Outline each Plasmodium falciparum-infected red blood cell.
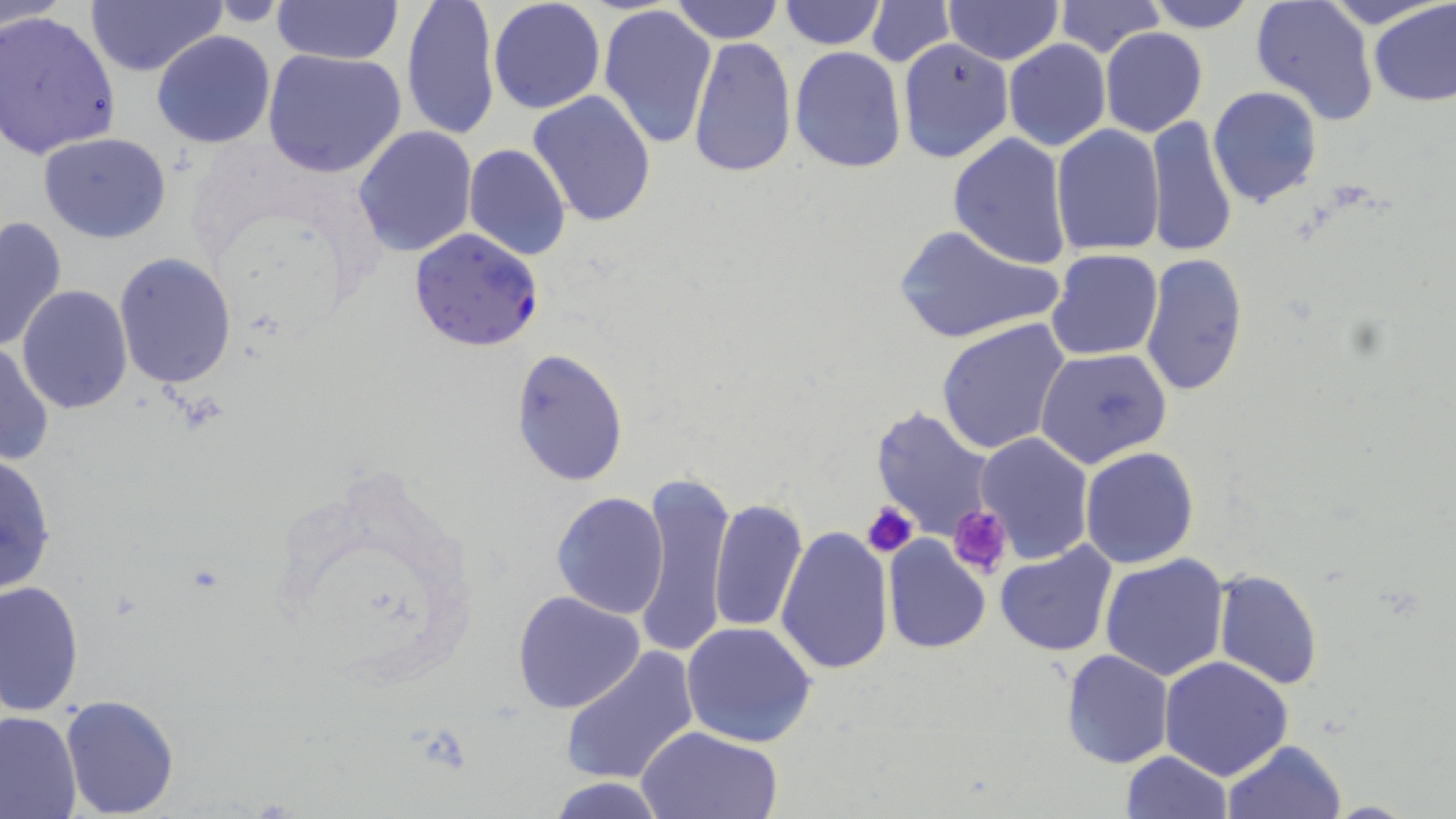
Approximate bounding boxes as (x1, y1, x2, y2) in pixels.
Plasmodium falciparum-infected red blood cells: (408, 227, 546, 352).

Uninfected red blood cell locations: (271, 0, 403, 67), (670, 0, 782, 44), (943, 0, 1063, 64), (1053, 0, 1168, 59), (1144, 0, 1259, 32), (1327, 0, 1445, 31), (1369, 0, 1456, 108), (0, 1, 69, 31), (85, 1, 222, 78), (400, 1, 500, 139), (488, 1, 605, 114), (779, 1, 886, 49), (865, 1, 955, 66), (1250, 1, 1380, 125), (204, 2, 295, 27), (599, 4, 718, 147), (0, 9, 122, 160), (1100, 27, 1209, 138), (150, 31, 277, 149), (687, 36, 796, 179), (896, 39, 1015, 163), (1004, 40, 1111, 152), (789, 45, 907, 173), (262, 47, 409, 179), (1208, 85, 1322, 208), (527, 91, 658, 229), (1145, 115, 1238, 258), (1050, 125, 1164, 256), (353, 126, 478, 256), (39, 132, 171, 242), (948, 132, 1072, 268), (463, 143, 570, 260), (0, 214, 68, 356), (893, 225, 1067, 344), (1045, 249, 1163, 362), (1139, 252, 1250, 399), (114, 254, 236, 390), (18, 285, 132, 414), (936, 318, 1072, 455), (0, 341, 53, 468), (1035, 347, 1172, 468), (510, 348, 629, 485), (872, 406, 999, 544), (975, 432, 1094, 563), (1080, 447, 1199, 568), (0, 453, 59, 596), (631, 467, 735, 662), (552, 492, 670, 617), (708, 497, 808, 635), (776, 523, 893, 675), (882, 535, 992, 657), (994, 541, 1118, 657), (1100, 553, 1231, 682), (1212, 569, 1323, 690), (0, 581, 85, 718), (512, 590, 646, 714), (681, 621, 818, 748), (559, 645, 700, 787), (1060, 648, 1174, 770), (1158, 656, 1292, 780), (60, 693, 179, 816), (0, 710, 82, 819), (636, 726, 783, 819), (1221, 739, 1347, 819), (1122, 750, 1233, 818), (547, 776, 669, 818). Platelet locations: (860, 500, 917, 559), (948, 505, 1011, 578). Slide-level diagnosis: Plasmodium falciparum. May-Grünwald-Giemsa-stained preparation. Light microscopy. Captured at 1000x magnification. Thin blood smear. One field of a larger specimen. Image is 1456×819 pixels.